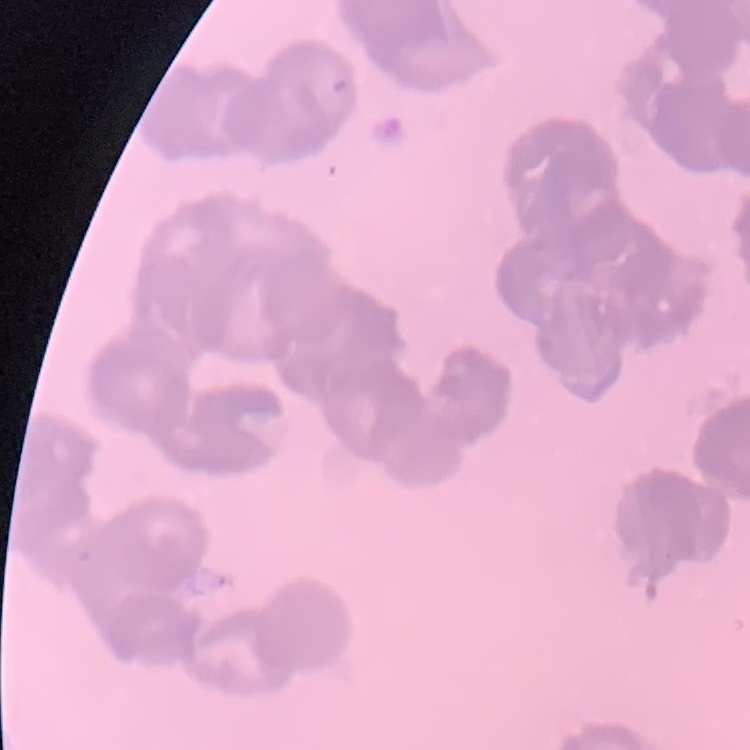
The erythrocytes exhibit rouleaux formation. Stained with either Field's or Giemsa. Thin blood smear. Square crop of a larger photomicrograph.